Report the malaria status.
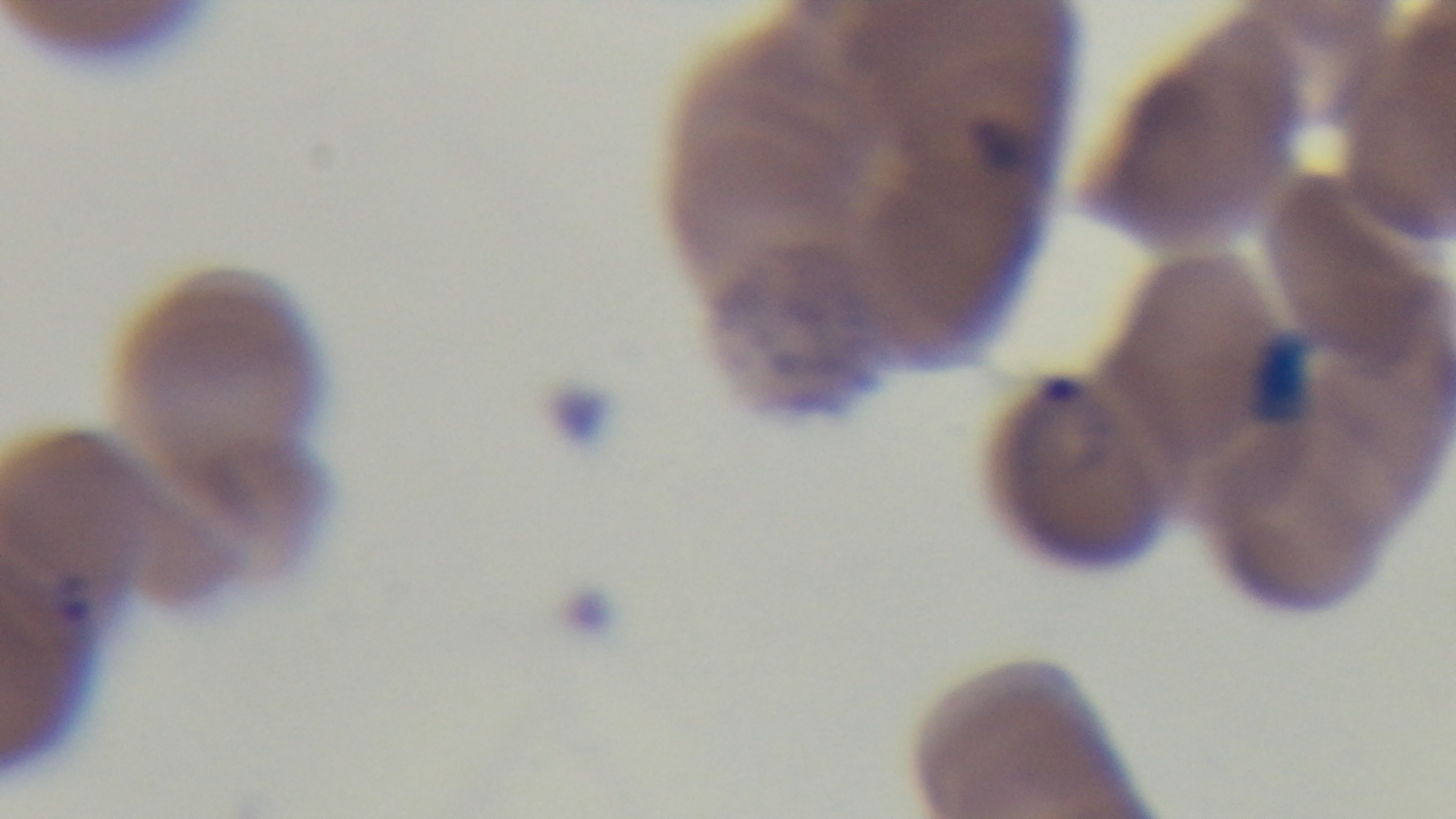

It is infected.

One field from the slide. Preparation: thin blood film. Oil-immersion objective, 100x. Mounted 4K digital camera. Light microscopy. Giemsa-stained.